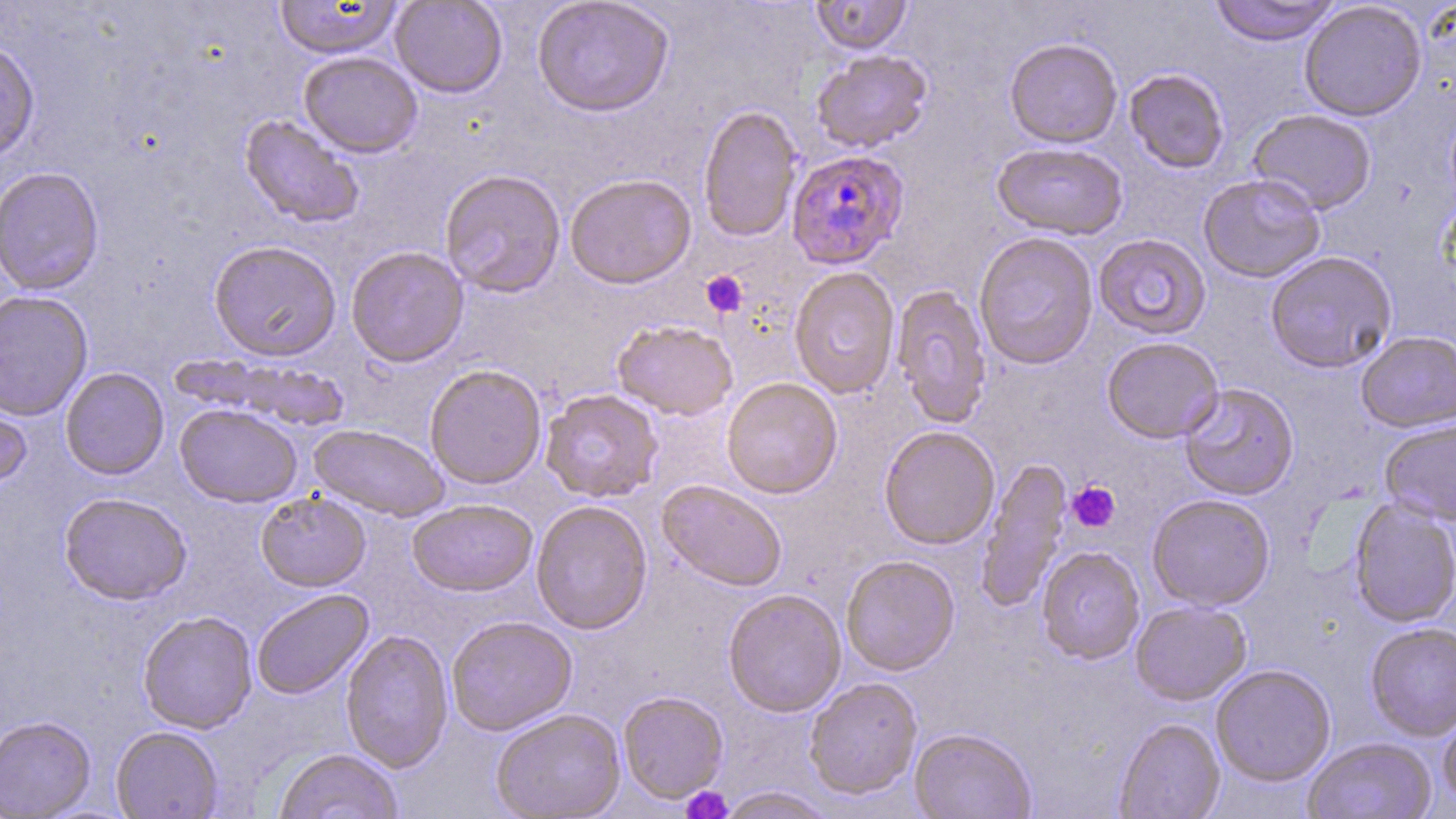 Approximate bounding boxes as named x1/y1/x2/y2 corners in pixels. Uninfected red blood cell locations: (x1=274, y1=0, x2=403, y2=60), (x1=390, y1=0, x2=507, y2=98), (x1=531, y1=0, x2=674, y2=118), (x1=809, y1=0, x2=913, y2=55), (x1=1208, y1=0, x2=1342, y2=46), (x1=1299, y1=1, x2=1427, y2=121), (x1=1004, y1=38, x2=1122, y2=149), (x1=0, y1=40, x2=40, y2=163), (x1=811, y1=49, x2=933, y2=153), (x1=298, y1=51, x2=423, y2=158), (x1=1124, y1=69, x2=1229, y2=174), (x1=698, y1=104, x2=803, y2=243), (x1=1247, y1=109, x2=1377, y2=215), (x1=239, y1=114, x2=365, y2=229), (x1=992, y1=141, x2=1127, y2=240), (x1=0, y1=166, x2=104, y2=295), (x1=439, y1=169, x2=566, y2=298), (x1=564, y1=174, x2=696, y2=289), (x1=1198, y1=174, x2=1326, y2=283), (x1=973, y1=232, x2=1099, y2=370), (x1=1094, y1=233, x2=1211, y2=340), (x1=208, y1=239, x2=341, y2=361), (x1=345, y1=246, x2=469, y2=367), (x1=1264, y1=251, x2=1398, y2=373), (x1=788, y1=267, x2=900, y2=400), (x1=891, y1=284, x2=992, y2=428), (x1=0, y1=290, x2=93, y2=421), (x1=612, y1=320, x2=738, y2=421), (x1=1356, y1=331, x2=1456, y2=433), (x1=1101, y1=337, x2=1224, y2=443), (x1=169, y1=352, x2=351, y2=427), (x1=425, y1=365, x2=547, y2=489), (x1=60, y1=367, x2=169, y2=480), (x1=721, y1=377, x2=843, y2=499), (x1=1179, y1=383, x2=1299, y2=501), (x1=0, y1=387, x2=32, y2=494), (x1=540, y1=389, x2=664, y2=503), (x1=175, y1=404, x2=302, y2=507), (x1=1379, y1=419, x2=1456, y2=526), (x1=309, y1=424, x2=449, y2=521), (x1=879, y1=426, x2=1000, y2=550), (x1=977, y1=457, x2=1072, y2=612), (x1=657, y1=480, x2=787, y2=593), (x1=255, y1=490, x2=371, y2=591), (x1=58, y1=492, x2=192, y2=605), (x1=1147, y1=494, x2=1275, y2=611), (x1=407, y1=499, x2=537, y2=597), (x1=1349, y1=499, x2=1456, y2=628), (x1=531, y1=500, x2=653, y2=634), (x1=1037, y1=546, x2=1145, y2=664), (x1=841, y1=555, x2=960, y2=676), (x1=251, y1=588, x2=374, y2=700), (x1=723, y1=589, x2=846, y2=717), (x1=1130, y1=600, x2=1252, y2=705), (x1=137, y1=610, x2=257, y2=733), (x1=446, y1=615, x2=577, y2=736), (x1=1365, y1=623, x2=1456, y2=741), (x1=340, y1=629, x2=454, y2=773), (x1=1211, y1=665, x2=1336, y2=787), (x1=804, y1=677, x2=923, y2=801), (x1=618, y1=691, x2=728, y2=803), (x1=1438, y1=707, x2=1456, y2=809), (x1=490, y1=709, x2=627, y2=819), (x1=0, y1=715, x2=96, y2=818), (x1=1114, y1=718, x2=1225, y2=819), (x1=111, y1=725, x2=224, y2=818), (x1=910, y1=729, x2=1036, y2=819), (x1=1302, y1=738, x2=1436, y2=819), (x1=274, y1=747, x2=404, y2=819), (x1=713, y1=787, x2=838, y2=818). Plasmodium falciparum-infected red blood cell locations: (x1=785, y1=149, x2=909, y2=270). Platelet locations: (x1=701, y1=270, x2=748, y2=317), (x1=1066, y1=481, x2=1120, y2=532), (x1=681, y1=786, x2=734, y2=819). Slide-level diagnosis: Plasmodium falciparum. May-Grünwald-Giemsa-stained preparation. Thin blood film. Image is 1456×819 pixels. Light microscopy. 1000x magnification. Single field of view.